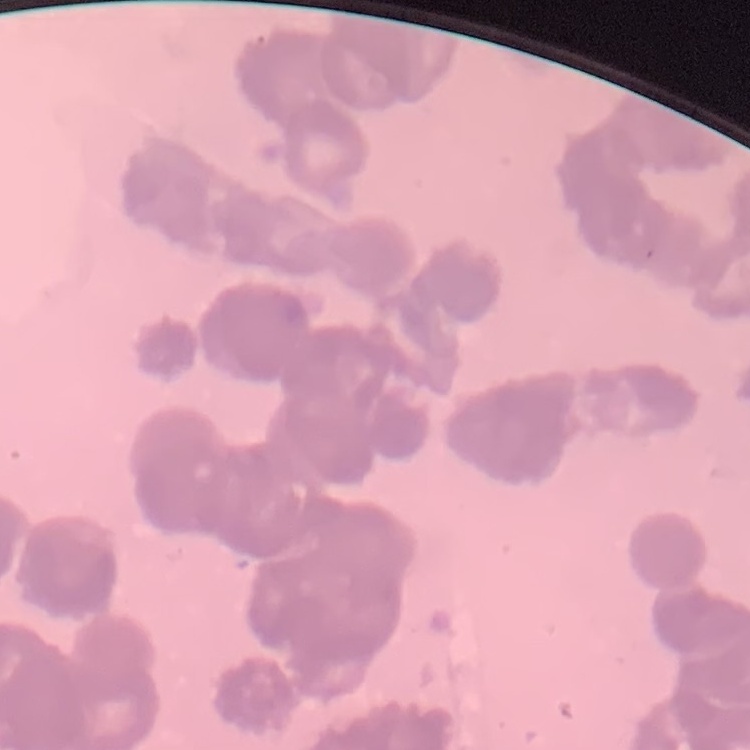 The red blood cells exhibit rouleaux formation. Thin blood film. One tile cut from a larger photomicrograph. Field's or Giemsa stain.